Locate every blood parasite and identify its species.
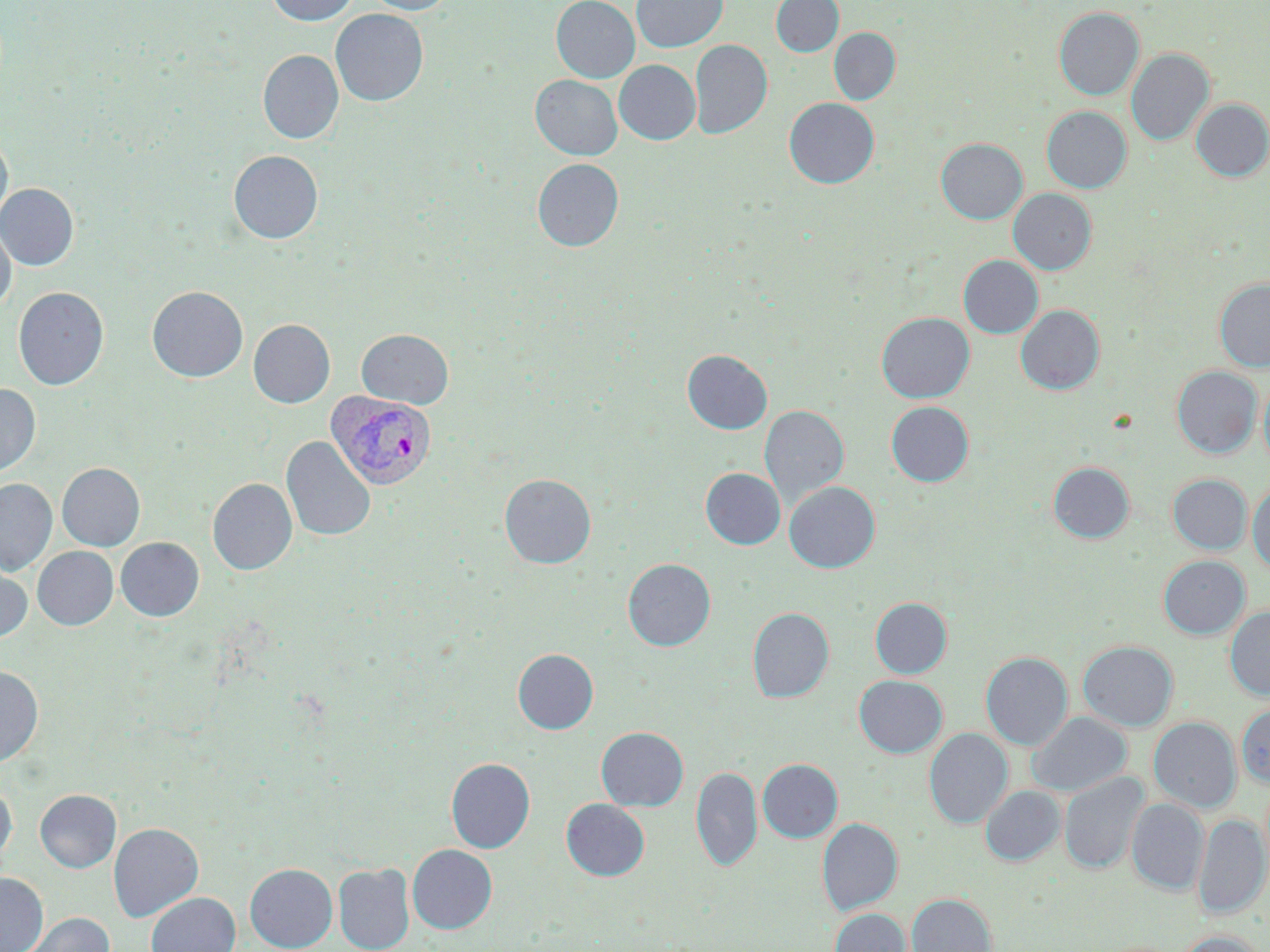

Approximate bounding boxes as (x1, y1, x2, y2) in pixels.
Plasmodium vivax-infected red blood cells: (326, 392, 437, 490).
No Plasmodium falciparum, Plasmodium ovale, Plasmodium malariae, Babesia divergens, or Trypanosoma brucei observed.

slide_level_diagnosis: Plasmodium vivax
image_size: 1270×952 pixels
magnification: 1000x
modality: light microscopy
preparation: thin blood smear
field_of_view: single
uninfected_red_blood_cell_locations: 'approximate bounding boxes as (x1, y1, x2, y2) in pixels: (266, 0, 360, 25), (362, 0, 456, 15), (551, 0, 639, 83), (632, 0, 728, 53), (771, 0, 843, 56), (1054, 7, 1144, 99), (330, 9, 428, 106), (829, 28, 900, 105), (690, 39, 772, 139), (1126, 48, 1214, 145), (257, 49, 343, 144), (614, 60, 700, 144), (530, 75, 622, 160), (784, 97, 879, 188), (1191, 98, 1270, 181), (1042, 106, 1131, 193), (0, 131, 13, 227), (936, 138, 1027, 224), (228, 150, 323, 244), (532, 158, 623, 252), (0, 183, 78, 270), (1008, 188, 1096, 274), (0, 221, 16, 312), (958, 255, 1043, 338), (1214, 278, 1270, 371), (146, 286, 249, 382), (13, 287, 108, 390), (1015, 305, 1104, 395), (876, 312, 974, 402), (248, 319, 335, 408), (357, 329, 454, 409), (682, 349, 772, 434), (1171, 366, 1261, 458), (1259, 376, 1270, 470), (0, 384, 40, 476), (886, 401, 974, 486), (759, 405, 849, 509), (282, 436, 375, 541), (1048, 462, 1134, 543), (57, 463, 145, 551), (700, 468, 786, 549), (499, 474, 596, 569), (1168, 474, 1252, 554), (0, 478, 57, 575), (207, 478, 297, 575), (784, 481, 880, 573), (1247, 482, 1270, 574), (116, 537, 204, 621), (33, 546, 118, 630), (1158, 555, 1250, 639), (623, 558, 715, 651), (0, 562, 32, 641), (870, 597, 952, 678), (1225, 606, 1270, 700), (747, 607, 834, 703), (1078, 640, 1178, 731), (513, 649, 598, 734), (980, 651, 1073, 750), (0, 664, 43, 767), (854, 675, 947, 757), (1236, 702, 1270, 788), (1027, 712, 1132, 796), (1149, 717, 1241, 812), (596, 726, 688, 811), (924, 728, 1013, 829), (446, 757, 535, 854), (757, 759, 843, 843), (691, 765, 762, 872), (1059, 772, 1148, 874), (0, 783, 16, 864), (981, 785, 1065, 866), (35, 789, 121, 872), (560, 798, 649, 880), (1127, 798, 1209, 894), (1193, 813, 1269, 918), (817, 817, 902, 915), (109, 822, 203, 921), (407, 844, 497, 934), (245, 863, 337, 951), (334, 863, 415, 952), (0, 872, 48, 952), (146, 892, 240, 952), (906, 893, 997, 952), (828, 908, 910, 952), (21, 912, 115, 951), (1175, 931, 1267, 952)'
stain: May-Grünwald-Giemsa